Identify the preparation type.
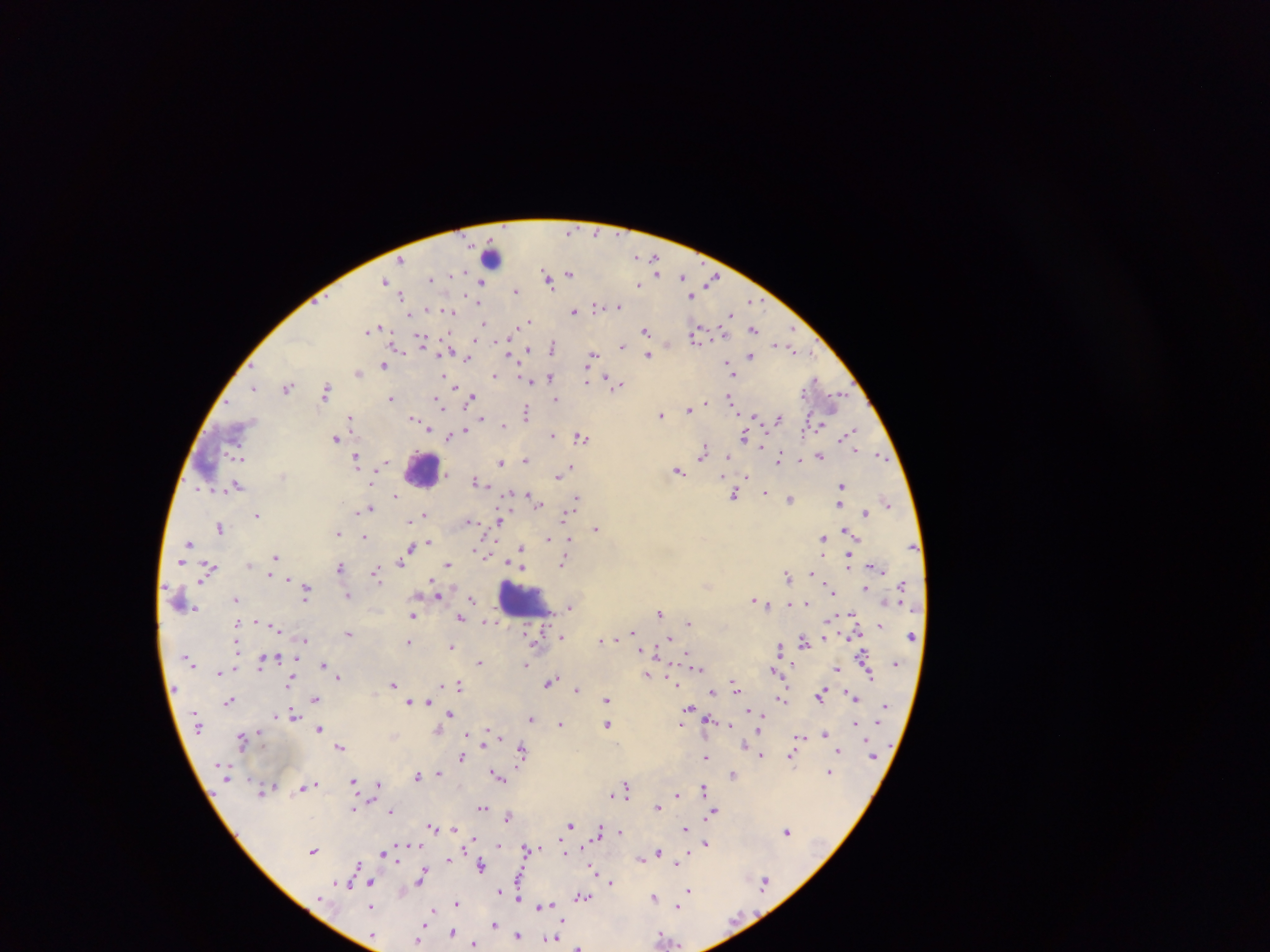

Thick blood smear.

Approximate centers as {x, y} in pixels.
Summary:
  - Malaria parasite locations: {571, 231}, {637, 257}, {401, 260}, {654, 260}, {656, 265}, {658, 271}, {570, 273}, {546, 275}, {452, 276}, {682, 276}, {431, 279}, {713, 280}, {384, 281}, {548, 281}, {480, 282}, {638, 285}, {516, 291}, {402, 295}, {691, 296}, {752, 301}, {596, 306}, {618, 306}, {573, 311}, {450, 313}, {730, 315}, {529, 320}, {484, 325}, {372, 328}, {754, 329}, {482, 330}, {646, 330}, {696, 335}, {422, 342}, {778, 344}, {621, 345}, {553, 347}, {528, 348}, {792, 348}, {509, 354}, {648, 355}, {751, 356}, {592, 357}, {468, 359}, {728, 363}, {383, 365}, {730, 371}, {357, 372}, {494, 375}, {444, 377}, {550, 377}, {586, 380}, {815, 380}, {528, 381}, {448, 382}, {617, 384}, {453, 385}, {254, 387}, {287, 387}, {326, 390}, {390, 398}, {471, 398}, {556, 399}, {729, 399}, {837, 400}, {439, 403}, {689, 410}, {527, 413}, {661, 415}, {755, 416}, {350, 418}, {414, 419}, {481, 419}, {777, 419}, {424, 425}, {503, 426}, {464, 431}, {850, 433}, {552, 435}, {744, 436}, {581, 437}, {449, 438}, {335, 439}, {704, 453}, {237, 455}, {819, 456}, {728, 457}, {881, 457}, {357, 458}, {778, 458}, {525, 460}, {800, 460}, {385, 462}, {501, 462}, {569, 467}, {679, 471}, {558, 476}, {476, 481}, {237, 486}, {841, 486}, {765, 492}, {395, 495}, {735, 495}, {531, 498}, {577, 498}, {791, 499}, {537, 502}, {887, 503}, {840, 504}, {368, 508}, {571, 509}, {865, 513}, {425, 514}, {257, 515}, {565, 515}, {411, 520}, {470, 521}, {499, 521}, {220, 528}, {596, 528}, {847, 532}, {338, 533}, {363, 537}, {548, 538}, {823, 538}, {429, 542}, {189, 543}, {409, 548}, {521, 548}, {477, 552}, {276, 557}, {404, 558}, {848, 560}, {564, 563}, {448, 565}, {521, 566}, {340, 567}, {209, 569}, {376, 573}, {815, 574}, {787, 576}, {306, 589}, {830, 589}, {865, 589}, {437, 593}, {348, 596}, {236, 599}, {472, 599}, {754, 600}, {790, 604}, {806, 605}, {570, 607}, {660, 612}, {413, 615}, {461, 618}, {489, 622}, {688, 623}, {880, 625}, {633, 632}, {348, 633}, {562, 636}, {668, 639}, {304, 640}, {601, 640}, {803, 640}, {410, 642}, {451, 646}, {780, 649}, {656, 651}, {863, 657}, {262, 662}, {479, 663}, {324, 664}, {526, 664}, {698, 667}, {773, 670}, {837, 670}, {220, 672}, {647, 675}, {338, 676}, {869, 676}, {290, 682}, {674, 682}, {550, 683}, {392, 684}, {734, 684}, {459, 685}, {559, 687}, {577, 689}, {712, 692}, {821, 694}, {853, 697}, {314, 698}, {781, 698}, {606, 699}, {229, 701}, {422, 701}, {410, 702}, {689, 708}, {293, 714}, {450, 715}, {531, 719}, {561, 724}, {608, 724}, {855, 724}, {728, 725}, {319, 729}, {825, 733}, {799, 737}, {242, 739}, {341, 746}, {839, 750}, {522, 751}, {761, 755}, {706, 757}, {462, 758}, {792, 759}, {829, 772}, {438, 773}, {733, 774}, {417, 775}, {498, 776}, {353, 782}, {314, 784}, {379, 785}, {307, 787}, {627, 788}, {704, 789}, {263, 791}, {677, 794}, {658, 807}, {481, 808}, {353, 809}, {391, 811}, {714, 811}, {508, 816}, {570, 826}, {432, 827}, {453, 828}, {685, 829}, {599, 831}, {787, 831}, {620, 832}, {706, 843}, {527, 849}, {313, 851}, {384, 853}, {658, 853}, {641, 858}, {679, 858}, {448, 859}, {677, 862}, {358, 865}, {481, 866}, {593, 869}, {422, 876}, {610, 882}, {369, 883}, {764, 883}, {689, 890}, {582, 896}, {519, 897}, {654, 897}, {457, 902}, {544, 905}, {371, 907}, {678, 907}, {430, 914}, {494, 924}, {452, 932}, {517, 935}, {419, 938}, {664, 938}, {550, 939}, {475, 944}, {579, 946}
  - Leukocyte locations: {492, 253}, {423, 470}, {522, 599}
  - Capture: mobile-phone photograph through a microscope
  - Field of view: single
  - Country: Ghana
  - Image size: 1270×952 pixels